Report the malaria status of this cell.
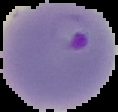

It is parasitized.

preparation = thin blood smear
image type = segmented cell region with the area outside set to black
image size = 118×112 pixels